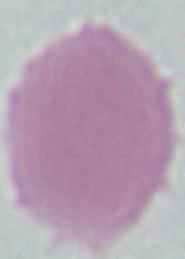

Photomicrograph. Captured at 1000x magnification. A red blood cell is seen.